Locate every blood parasite and identify its species.
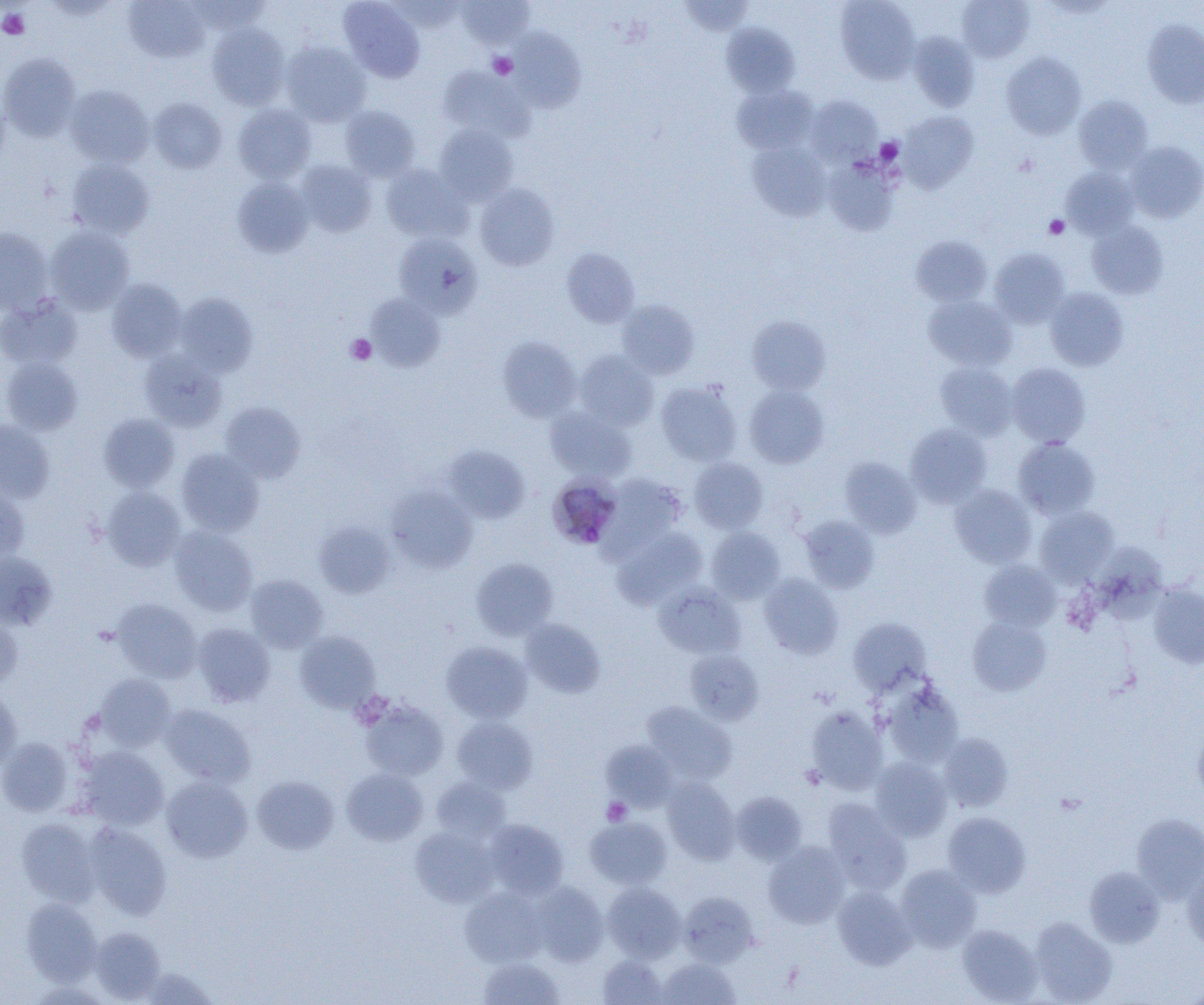

Approximate bounding boxes as (x1, y1, x2, y2) in pixels.
Plasmodium malariae-infected red blood cells: (548, 473, 628, 548).
No Plasmodium falciparum, Plasmodium ovale, Plasmodium vivax, Babesia divergens, or Trypanosoma brucei observed.

slide-level diagnosis = Plasmodium malariae
platelet locations = approximate bounding boxes as (x1, y1, x2, y2) in pixels: (0, 9, 29, 39), (489, 53, 517, 79), (876, 138, 904, 164), (1044, 215, 1070, 239), (346, 334, 376, 365), (602, 798, 632, 826)
modality = optical microscopy
field of view = one of a larger specimen
image size = 1204×1005 pixels
magnification = 1000x
uninfected red blood cell locations = approximate bounding boxes as (x1, y1, x2, y2) in pixels: (185, 0, 270, 33), (338, 0, 425, 83), (389, 0, 465, 32), (457, 0, 535, 49), (679, 0, 754, 36), (836, 0, 920, 84), (957, 0, 1034, 62), (123, 1, 208, 63), (1142, 19, 1204, 108), (720, 22, 799, 96), (207, 24, 290, 109), (508, 27, 586, 112), (908, 31, 979, 111), (281, 42, 370, 126), (0, 52, 81, 141), (1001, 52, 1086, 140), (438, 66, 535, 143), (732, 84, 818, 154), (64, 85, 154, 168), (806, 95, 882, 166), (1073, 95, 1153, 173), (148, 98, 227, 174), (233, 104, 316, 184), (340, 105, 420, 181), (898, 111, 978, 193), (435, 124, 518, 205), (748, 141, 831, 221), (1125, 141, 1204, 223), (67, 158, 155, 239), (824, 158, 901, 236), (295, 160, 377, 237), (381, 164, 470, 243), (1062, 167, 1139, 238), (233, 177, 313, 257), (474, 183, 560, 271), (1086, 221, 1169, 300), (0, 226, 53, 313), (46, 227, 134, 314), (393, 234, 483, 318), (911, 235, 993, 306), (561, 248, 640, 328), (989, 248, 1070, 328), (106, 279, 187, 362), (1045, 288, 1129, 371), (174, 293, 257, 376), (365, 293, 446, 372), (0, 295, 82, 370), (923, 295, 1018, 371), (617, 299, 700, 379), (746, 316, 831, 395), (498, 337, 581, 423), (139, 350, 227, 432), (574, 350, 658, 430), (1, 357, 83, 436), (936, 362, 1018, 439), (1007, 363, 1090, 447), (655, 380, 743, 466), (744, 385, 829, 468), (220, 402, 306, 483), (545, 407, 636, 483), (98, 413, 180, 491), (0, 420, 55, 503), (905, 423, 991, 507), (1013, 437, 1100, 519), (443, 444, 530, 523), (176, 448, 264, 536), (839, 457, 921, 538), (689, 458, 768, 534), (601, 473, 688, 555), (950, 484, 1037, 568), (0, 486, 29, 563), (101, 486, 186, 571), (386, 486, 478, 573), (1035, 506, 1119, 586), (799, 514, 879, 593), (314, 522, 394, 598), (169, 526, 258, 616), (612, 526, 707, 609), (706, 527, 785, 603), (1093, 540, 1178, 621), (0, 551, 57, 630), (471, 558, 558, 640), (979, 559, 1061, 631), (758, 573, 843, 659), (245, 574, 328, 652), (654, 583, 745, 659), (1147, 583, 1204, 669), (111, 598, 202, 682), (0, 613, 22, 691), (967, 616, 1052, 696), (519, 618, 606, 698), (847, 618, 931, 695), (193, 623, 276, 706), (294, 630, 380, 712), (441, 641, 532, 723), (684, 649, 764, 725), (94, 673, 176, 751), (880, 680, 963, 767), (0, 689, 22, 774), (360, 700, 449, 780), (642, 702, 737, 785), (160, 704, 256, 787), (805, 707, 888, 794), (452, 716, 538, 794), (1193, 726, 1204, 800), (939, 733, 1013, 812), (0, 737, 73, 816), (601, 740, 678, 811), (79, 745, 169, 830), (870, 758, 952, 841), (341, 768, 428, 846), (161, 775, 253, 863), (251, 775, 339, 854), (662, 776, 740, 864), (431, 777, 511, 842), (731, 791, 807, 865), (822, 798, 911, 893), (942, 811, 1031, 896), (1132, 813, 1204, 902), (585, 816, 672, 889), (16, 818, 99, 905), (485, 819, 569, 899), (84, 823, 172, 919), (410, 826, 500, 907), (763, 841, 850, 928), (1182, 862, 1204, 951), (896, 864, 982, 952), (1084, 867, 1164, 948), (530, 881, 608, 967), (602, 882, 686, 962), (833, 886, 915, 969), (460, 887, 547, 967), (678, 891, 758, 967), (21, 898, 101, 985), (1029, 917, 1117, 1004), (957, 924, 1042, 1004), (89, 926, 166, 1002), (597, 954, 668, 1004), (478, 957, 565, 1004), (656, 957, 740, 1004), (136, 967, 220, 1004)
preparation = thin blood film